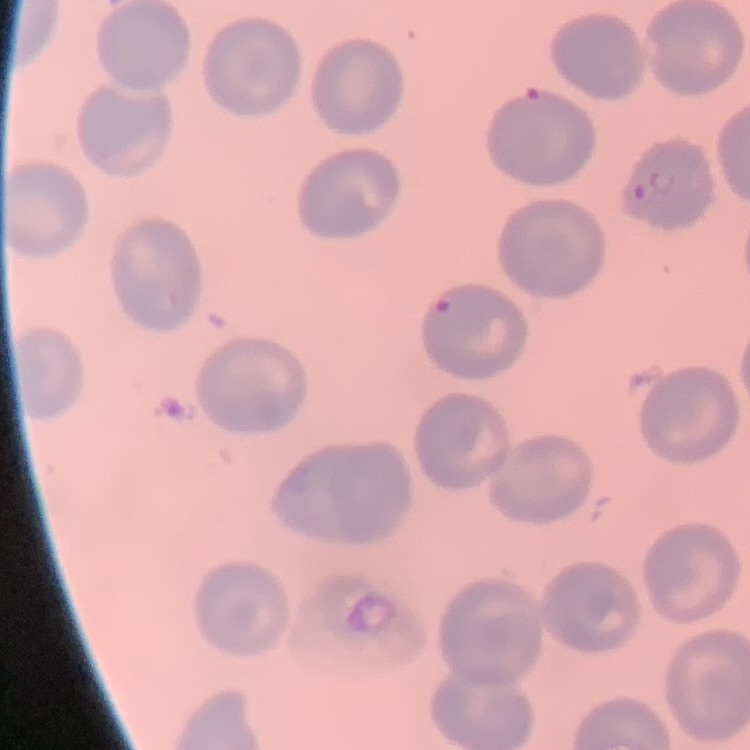

Summary:
  - Red blood cell morphology: no rouleaux formation
  - Stain: Field's or Giemsa
  - Image type: square crop of a larger photomicrograph
  - Preparation: thin blood film